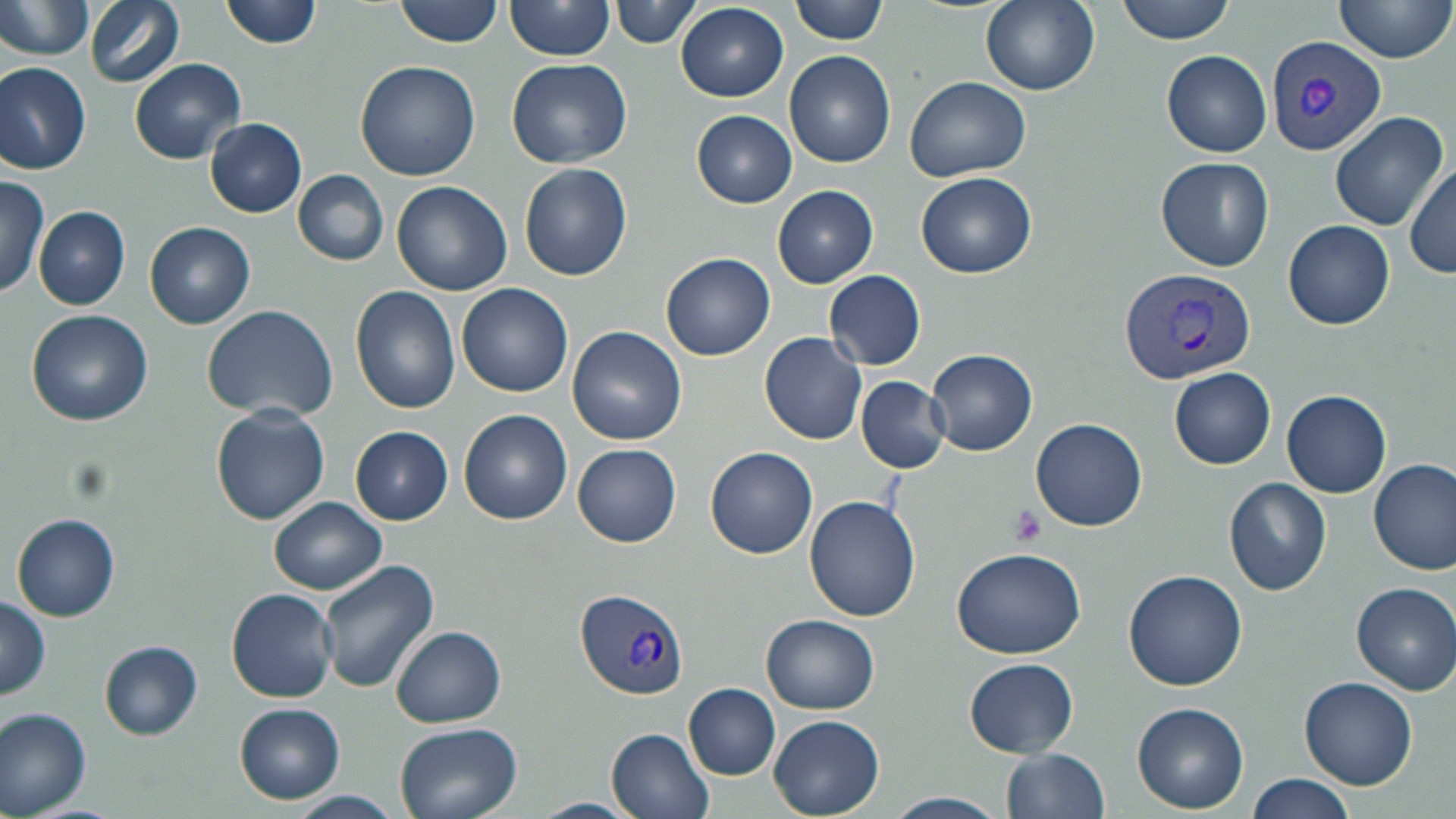

Summary:
  - Coordinate format: approximate bounding boxes as (x1, y1, x2, y2) in pixels
  - Platelet locations: (1009, 505, 1048, 546)
  - Uninfected red blood cell locations: (0, 0, 98, 62), (86, 0, 185, 88), (223, 0, 321, 48), (396, 0, 504, 47), (506, 0, 616, 59), (792, 0, 890, 44), (980, 0, 1101, 95), (1116, 0, 1239, 43), (613, 1, 702, 48), (1332, 1, 1456, 67), (675, 3, 789, 102), (1162, 50, 1271, 157), (786, 51, 896, 169), (506, 57, 633, 168), (131, 58, 245, 163), (357, 61, 481, 181), (0, 63, 91, 174), (905, 75, 1032, 182), (692, 110, 797, 207), (1329, 110, 1448, 231), (206, 117, 308, 217), (1156, 156, 1274, 272), (1407, 161, 1456, 278), (518, 162, 632, 280), (293, 168, 390, 266), (916, 172, 1038, 279), (0, 176, 50, 301), (391, 180, 512, 296), (773, 185, 879, 288), (35, 205, 131, 309), (1284, 219, 1395, 329), (145, 222, 254, 329), (662, 252, 775, 360), (826, 270, 926, 370), (458, 283, 572, 397), (351, 286, 462, 414), (202, 304, 339, 421), (27, 310, 154, 425), (566, 325, 686, 444), (759, 332, 867, 444), (925, 349, 1037, 456), (1171, 367, 1276, 470), (857, 378, 948, 472), (1282, 390, 1391, 498), (211, 405, 330, 524), (460, 410, 571, 526), (1030, 418, 1148, 532), (350, 426, 454, 525), (573, 443, 682, 546), (706, 446, 818, 559), (1369, 458, 1456, 576), (1224, 477, 1333, 595), (268, 497, 387, 595), (804, 497, 921, 622), (13, 513, 121, 620), (950, 546, 1088, 660), (318, 560, 439, 693), (1125, 569, 1247, 690), (1350, 581, 1456, 694), (226, 589, 337, 702), (0, 596, 51, 701), (762, 616, 879, 714), (392, 626, 504, 727), (99, 640, 203, 739), (964, 658, 1078, 757), (1300, 675, 1417, 789), (685, 683, 781, 779), (1134, 703, 1249, 813), (235, 704, 345, 802), (0, 706, 94, 816), (769, 715, 884, 816), (394, 722, 524, 819), (606, 726, 716, 819), (1001, 748, 1110, 819), (1244, 773, 1355, 819), (290, 791, 402, 819), (881, 791, 1008, 819), (532, 797, 640, 818)
  - Plasmodium vivax-infected red blood cell locations: (1266, 34, 1387, 156), (1119, 266, 1254, 386), (575, 588, 691, 699)
  - Slide-level diagnosis: Plasmodium vivax
  - Modality: optical microscopy
  - Image size: 1456×819 pixels
  - Field of view: single
  - Preparation: thin blood smear
  - Stain: May-Grünwald-Giemsa
  - Magnification: 1000x